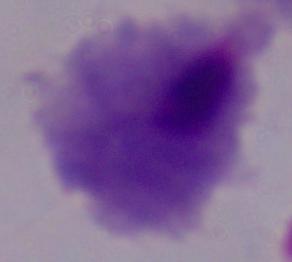 A trichomonad is shown. 1000x magnification. Micrograph.